State which parasite is depicted.
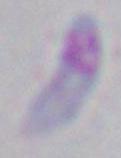

Toxoplasma gondii.

modality = photomicrograph
magnification = 1000x